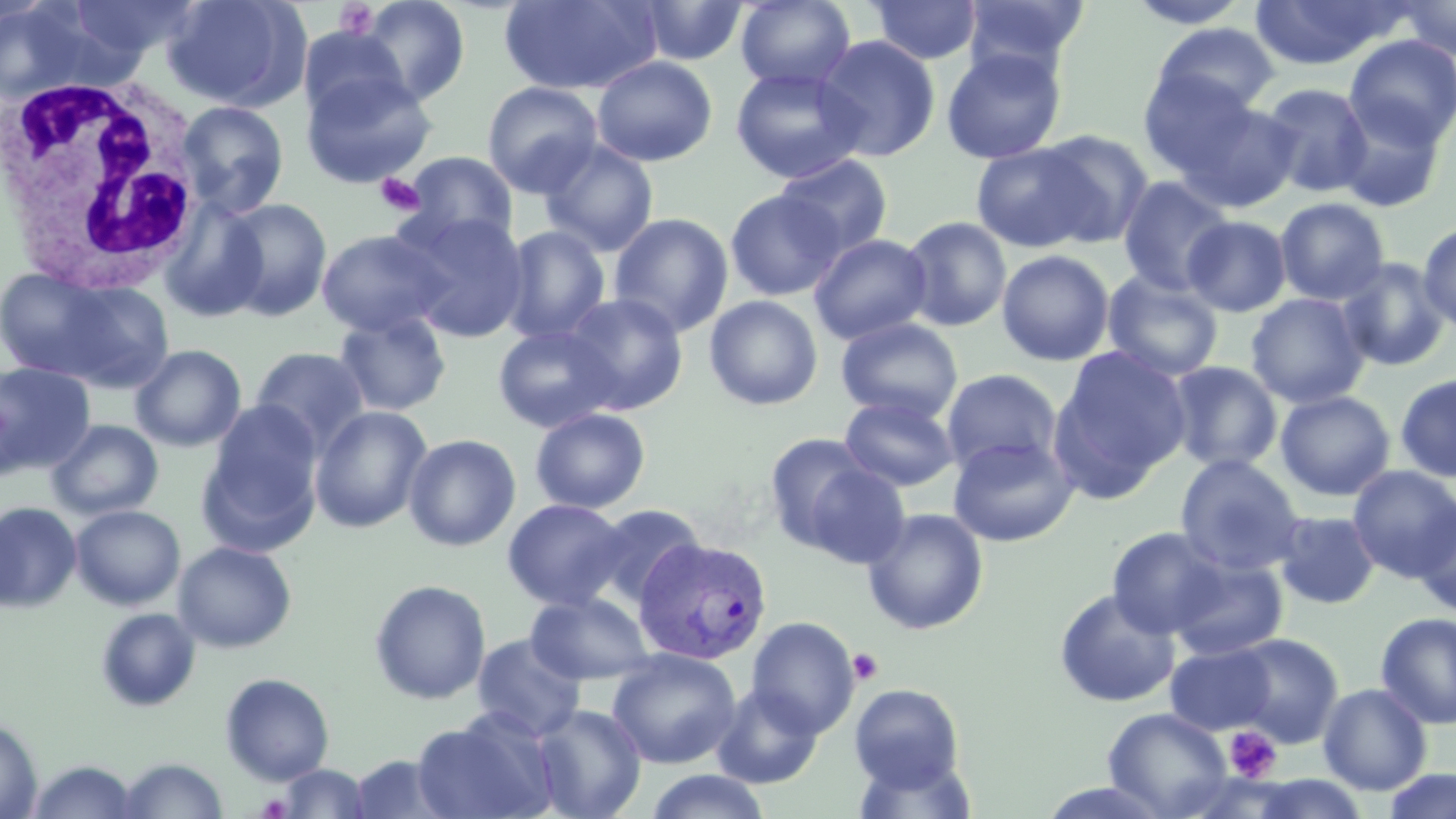
Approximate bounding boxes as (x1,y1)-(x2,y2) corner pairs in pixels. White blood cell locations: (1,73)-(209,291). Plasmodium vivax-infected red blood cell locations: (633,538)-(773,665). Platelet locations: (332,2)-(381,40), (375,172)-(425,216), (847,647)-(884,685), (1224,725)-(1282,783), (256,793)-(293,818). Uninfected red blood cell locations: (66,0)-(200,63), (162,0)-(307,111), (735,0)-(856,92), (960,0)-(1089,79), (1393,0)-(1456,60), (0,1)-(113,103), (355,1)-(472,107), (500,1)-(660,95), (635,1)-(750,67), (868,1)-(982,65), (1125,1)-(1251,29), (1250,1)-(1398,70), (1151,23)-(1280,119), (297,26)-(412,123), (814,35)-(941,162), (1344,35)-(1456,148), (941,47)-(1067,164), (591,56)-(718,167), (729,66)-(868,184), (1138,68)-(1260,179), (300,69)-(437,188), (482,80)-(604,197), (1259,83)-(1373,198), (1334,98)-(1447,213), (1181,99)-(1300,210), (174,100)-(290,218), (1036,129)-(1154,247), (538,140)-(659,256), (970,142)-(1101,252), (401,151)-(519,247), (775,154)-(894,256), (1117,176)-(1234,297), (724,189)-(845,301), (159,196)-(269,322), (1275,197)-(1390,305), (220,198)-(332,321), (398,210)-(531,343), (608,212)-(733,337), (1183,215)-(1292,317), (901,216)-(1012,332), (1418,220)-(1456,333), (500,226)-(611,345), (316,228)-(452,338), (809,233)-(933,344), (996,249)-(1115,366), (1335,257)-(1451,371), (4,268)-(169,389), (1103,271)-(1223,382), (562,293)-(689,414), (1246,293)-(1370,409), (704,295)-(823,411), (333,311)-(452,417), (836,317)-(963,423), (493,323)-(621,433), (130,344)-(246,452), (1048,345)-(1191,498), (249,346)-(370,455), (0,361)-(95,477), (1166,361)-(1282,473), (940,369)-(1064,477), (1395,372)-(1456,482), (1275,390)-(1396,501), (839,395)-(959,492), (201,403)-(323,552), (309,405)-(433,533), (530,407)-(651,514), (47,419)-(163,520), (403,433)-(521,552), (763,433)-(884,553), (947,435)-(1080,547), (1175,454)-(1305,575), (798,461)-(911,567), (1348,465)-(1456,581), (502,498)-(630,610), (0,502)-(82,612), (1412,502)-(1456,617), (588,503)-(706,608), (70,504)-(186,610), (862,508)-(989,635), (1273,510)-(1381,610), (1107,527)-(1229,638), (173,541)-(297,653), (1169,555)-(1288,661), (369,579)-(492,705), (1054,587)-(1180,707), (525,592)-(656,685), (95,607)-(200,711), (1375,612)-(1456,729), (745,616)-(860,738), (471,633)-(587,741), (1228,633)-(1343,747), (1164,643)-(1277,735), (606,648)-(741,769), (221,673)-(335,784), (848,683)-(966,793), (1318,683)-(1433,795), (711,684)-(825,789), (531,703)-(647,819), (1103,707)-(1232,818), (412,712)-(558,819), (0,717)-(42,818), (348,754)-(453,818), (116,757)-(228,818), (26,759)-(141,818), (275,763)-(372,818), (1382,769)-(1456,819), (642,770)-(774,819), (1245,775)-(1373,818). Slide-level diagnosis: Plasmodium vivax. Optical microscopy. One field of a larger specimen. Image is 1456×819 pixels. Thin blood film. Captured at 1000x magnification. May-Grünwald-Giemsa-stained preparation.